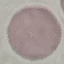
malaria status = uninfected
preparation = thin blood film
stain = Giemsa
image type = automatically extracted cell patch, resized to 64 × 64 pixels
capture = smartphone through the microscope eyepiece